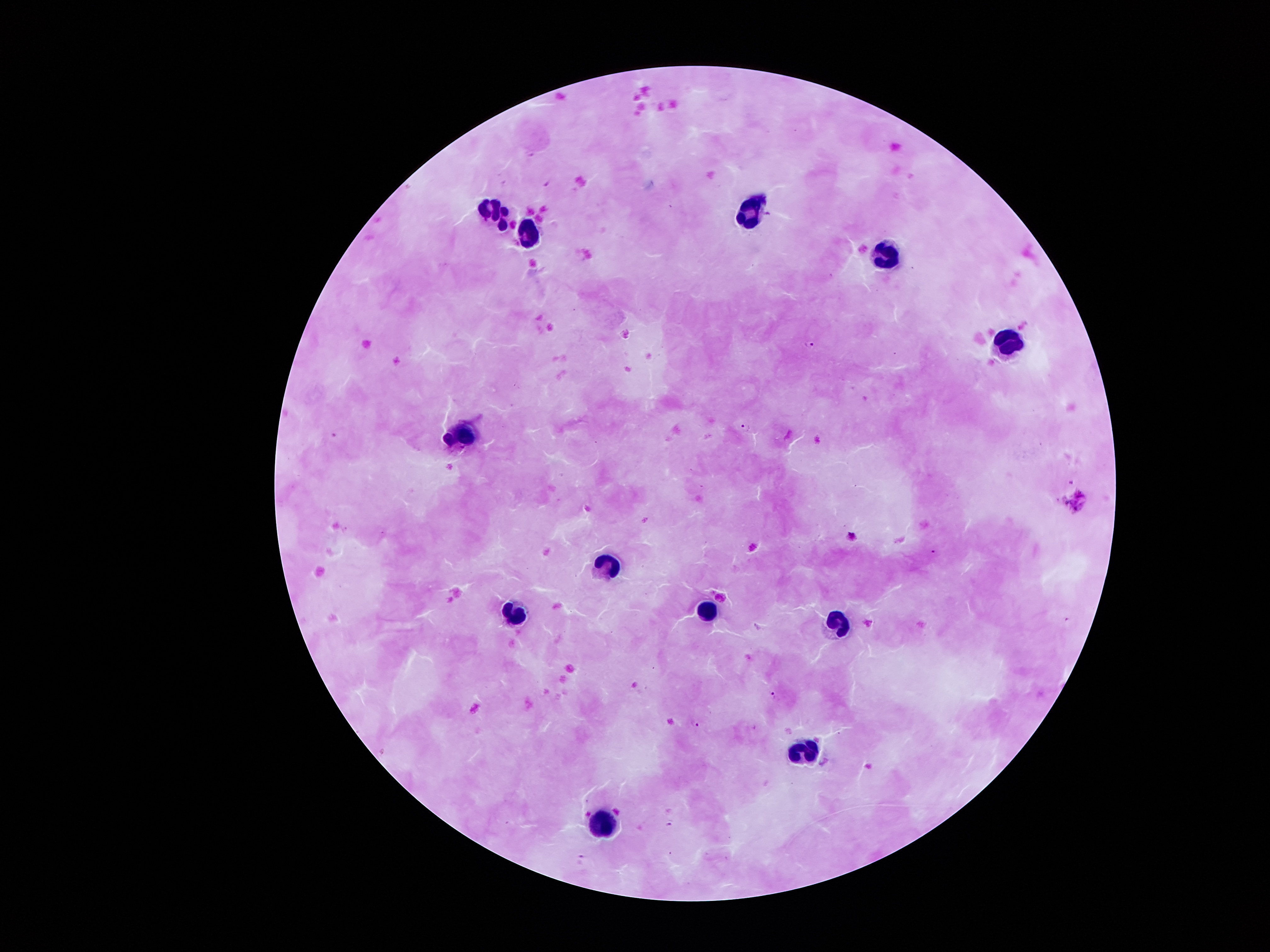 Approximate centers as [x, y] in pixels. Plasmodium parasite locations: [547, 183], [812, 344], [746, 427], [851, 534], [774, 696], [696, 724], [670, 824], [582, 855]. Leukocyte locations: [754, 212], [494, 213], [528, 236], [882, 258], [1011, 342], [458, 431], [608, 565], [705, 604], [509, 614], [839, 620], [807, 748], [602, 819]. Smartphone photograph taken through the microscope eyepiece. Image is 1270×952 pixels. One field from this slide. Patient malaria status: positive for Plasmodium falciparum. Giemsa-stained preparation. Thick blood smear. 100x magnification.